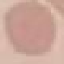

Malaria status: uninfected. Cell patch, automatically extracted from a larger field of view and resized to 64 × 64 pixels. Thin smear of blood. Photographed with a smartphone camera at the microscope eyepiece. Giemsa stain.